Locate every blood parasite and identify its species.
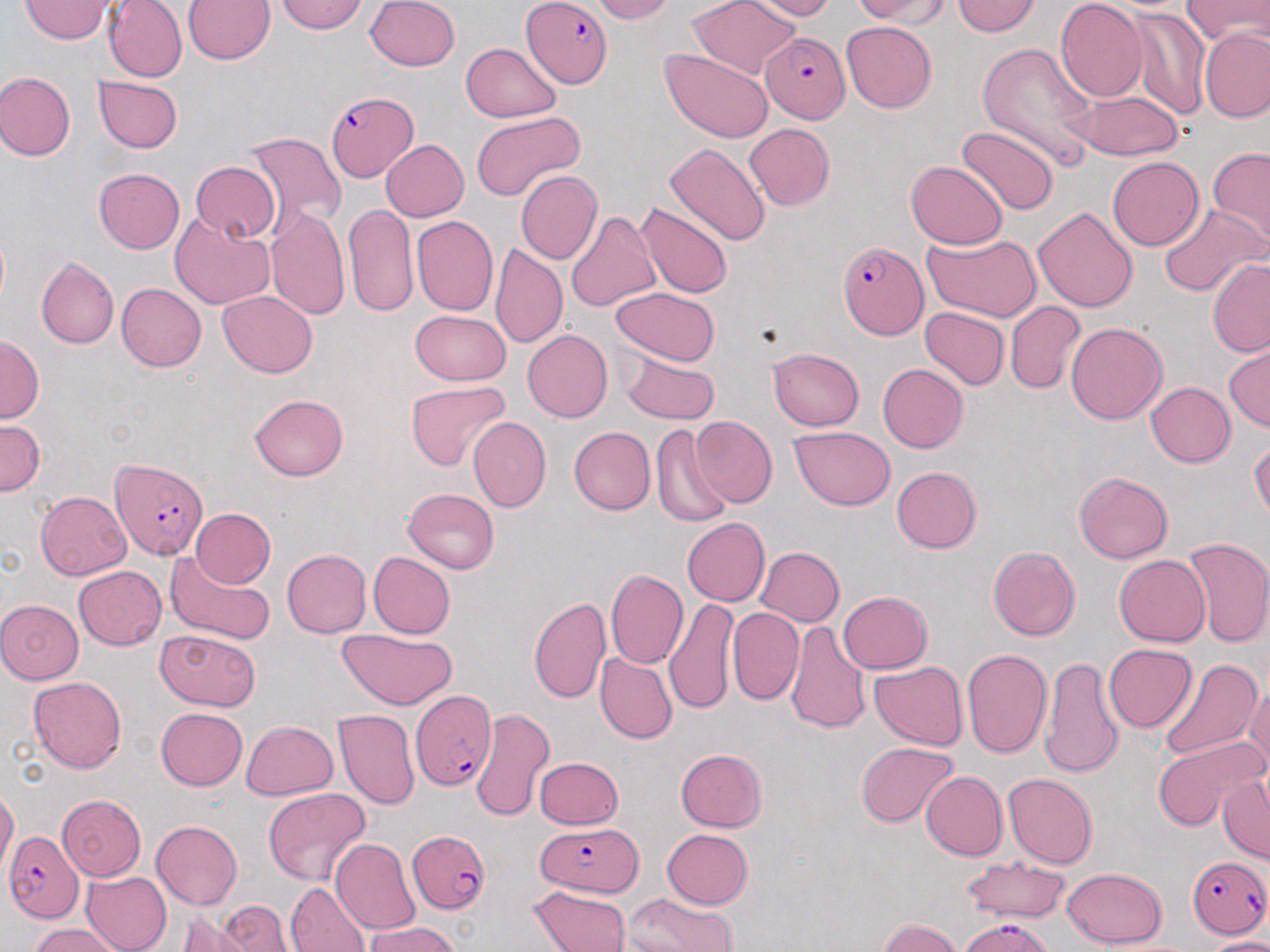

Approximate bounding boxes as [x1, y1, x2, y2] in pixels.
Plasmodium falciparum-infected red blood cells: [521, 1, 615, 87], [759, 33, 848, 122], [328, 91, 423, 181], [837, 240, 928, 341], [111, 454, 208, 559], [409, 686, 498, 792], [535, 821, 643, 896], [406, 830, 491, 915], [3, 832, 83, 923], [1187, 856, 1269, 939], [958, 918, 1055, 952].
No Plasmodium ovale, Plasmodium malariae, Plasmodium vivax, Babesia divergens, or Trypanosoma brucei observed.

Uninfected red blood cell locations: [106, 0, 185, 81], [184, 0, 276, 65], [273, 0, 370, 35], [363, 0, 461, 72], [585, 0, 674, 23], [687, 0, 799, 79], [752, 0, 838, 19], [846, 0, 954, 24], [953, 0, 1042, 37], [1056, 0, 1146, 102], [1183, 0, 1268, 48], [22, 1, 112, 43], [1127, 8, 1209, 120], [841, 23, 938, 112], [1200, 27, 1270, 123], [463, 40, 563, 121], [975, 42, 1098, 162], [661, 50, 775, 143], [0, 71, 75, 160], [94, 76, 182, 154], [1075, 88, 1183, 158], [471, 111, 589, 201], [743, 124, 835, 210], [956, 128, 1057, 216], [244, 131, 348, 233], [380, 138, 468, 221], [664, 143, 771, 249], [1205, 146, 1270, 245], [1106, 158, 1202, 251], [905, 161, 1007, 250], [189, 162, 279, 242], [93, 166, 185, 253], [517, 170, 602, 266], [634, 201, 733, 300], [1155, 201, 1267, 303], [1032, 203, 1138, 313], [344, 204, 419, 316], [566, 209, 660, 315], [267, 210, 351, 323], [170, 213, 277, 307], [410, 215, 498, 317], [920, 233, 1042, 322], [492, 245, 568, 350], [36, 257, 118, 349], [1208, 257, 1270, 356], [116, 281, 207, 373], [609, 286, 721, 364], [216, 291, 319, 377], [1004, 300, 1084, 393], [921, 306, 1008, 390], [411, 309, 512, 387], [1066, 321, 1167, 426], [520, 330, 612, 423], [1, 335, 43, 426], [769, 348, 864, 431], [1224, 348, 1269, 432], [619, 355, 722, 424], [877, 363, 968, 452], [404, 380, 510, 469], [1146, 382, 1236, 468], [249, 393, 350, 483], [692, 416, 777, 506], [470, 417, 550, 512], [0, 419, 43, 496], [649, 422, 733, 530], [566, 426, 655, 515], [790, 427, 895, 511], [1250, 437, 1269, 525], [892, 466, 982, 553], [1074, 470, 1171, 565], [401, 487, 501, 574], [35, 491, 133, 579], [189, 508, 275, 588], [681, 517, 769, 608], [1180, 535, 1270, 648], [756, 546, 845, 628], [989, 546, 1080, 643], [280, 549, 371, 638], [161, 550, 276, 647], [369, 550, 457, 638], [1114, 554, 1210, 648], [74, 566, 166, 650], [604, 568, 688, 669], [836, 590, 932, 674], [529, 593, 610, 702], [0, 597, 84, 682], [666, 600, 737, 713], [727, 609, 804, 706], [786, 619, 870, 733], [155, 628, 263, 711], [335, 629, 458, 709], [1104, 644, 1196, 732], [960, 647, 1054, 760], [599, 653, 677, 743], [1041, 656, 1123, 777], [1155, 657, 1262, 766], [869, 660, 969, 750], [30, 675, 126, 773], [1244, 684, 1270, 780], [155, 708, 248, 791], [468, 708, 554, 823], [333, 710, 418, 810], [240, 719, 339, 801], [1152, 733, 1267, 834], [855, 741, 958, 827], [675, 747, 769, 831], [533, 756, 623, 831], [919, 771, 1005, 860], [1004, 773, 1096, 869], [1216, 775, 1269, 860], [261, 787, 373, 886], [0, 788, 19, 875], [58, 795, 145, 878], [151, 819, 242, 907], [660, 828, 753, 909], [330, 840, 419, 935], [958, 855, 1071, 922], [1060, 867, 1168, 948], [83, 869, 174, 952], [286, 881, 369, 952], [528, 885, 631, 952], [624, 893, 743, 952], [217, 898, 289, 952], [179, 908, 253, 950], [875, 918, 962, 952], [361, 920, 464, 952], [25, 924, 124, 952], [1206, 932, 1270, 951]. Slide-level diagnosis: Plasmodium falciparum. Light microscopy. Thin blood smear. Image is 1270×952 pixels. May-Grünwald-Giemsa stain. 1000x magnification. Single field of view.